Assess the morphology of the red blood cells.
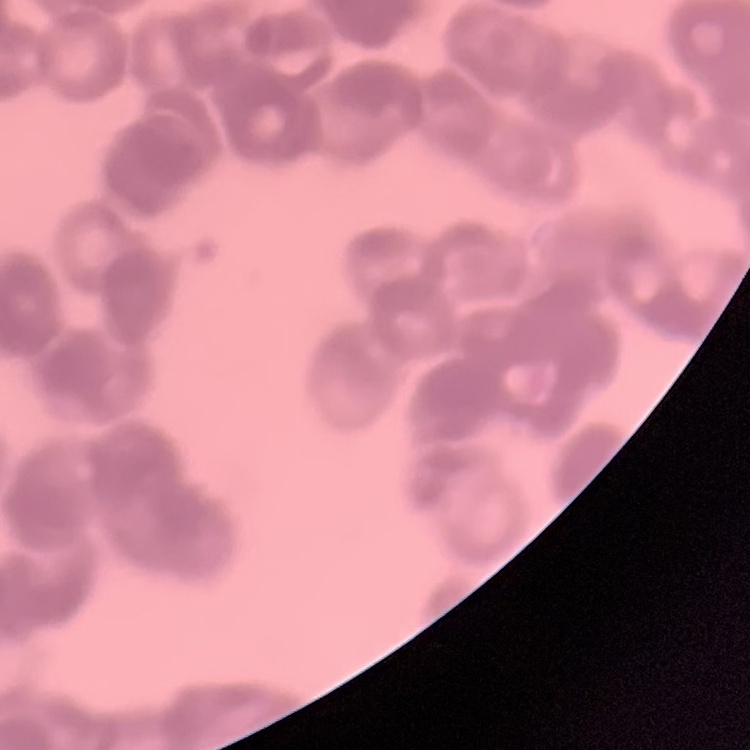

Rouleaux formation.

image_type: one tile cut from a larger photomicrograph
stain: Field's or Giemsa
preparation: thin blood film